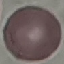

malaria status = uninfected
preparation = thin blood smear
capture = smartphone camera at the microscope eyepiece
stain = Giemsa
image type = automatically extracted cell patch, resized to 64 × 64 pixels